Look for Plasmodium parasites.
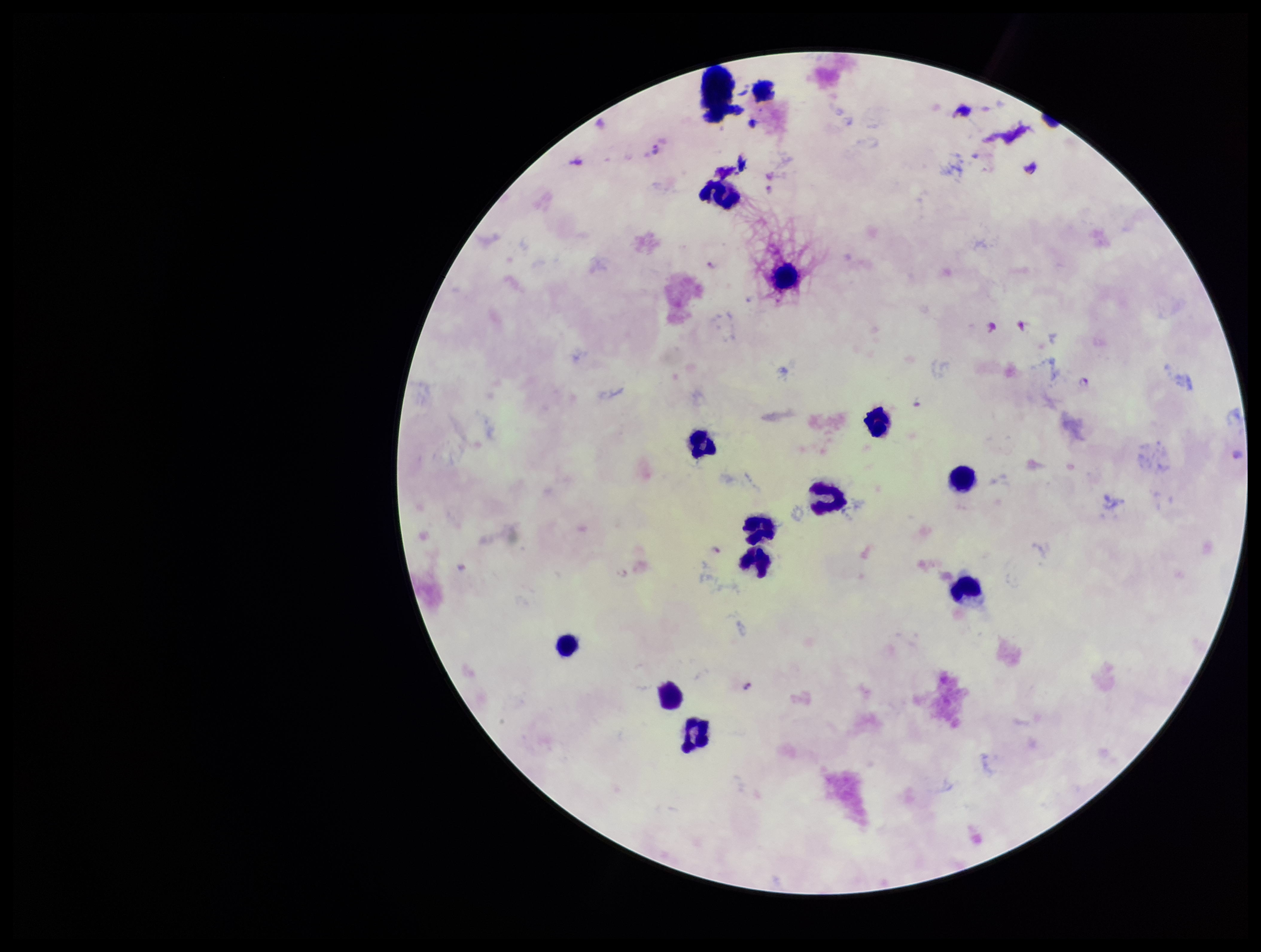
Seen.

Summary:
  - Patient malaria status: positive
  - Stain: Giemsa
  - Field of view: single
  - Image size: 1261×952 pixels
  - Species reported for this patient: Plasmodium falciparum
  - Leukocyte count: 13
  - Parasite count: 10
  - Capture: smartphone photograph through the microscope eyepiece
  - Preparation: thick smear